Locate every Plasmodium vivax-infected red blood cell.
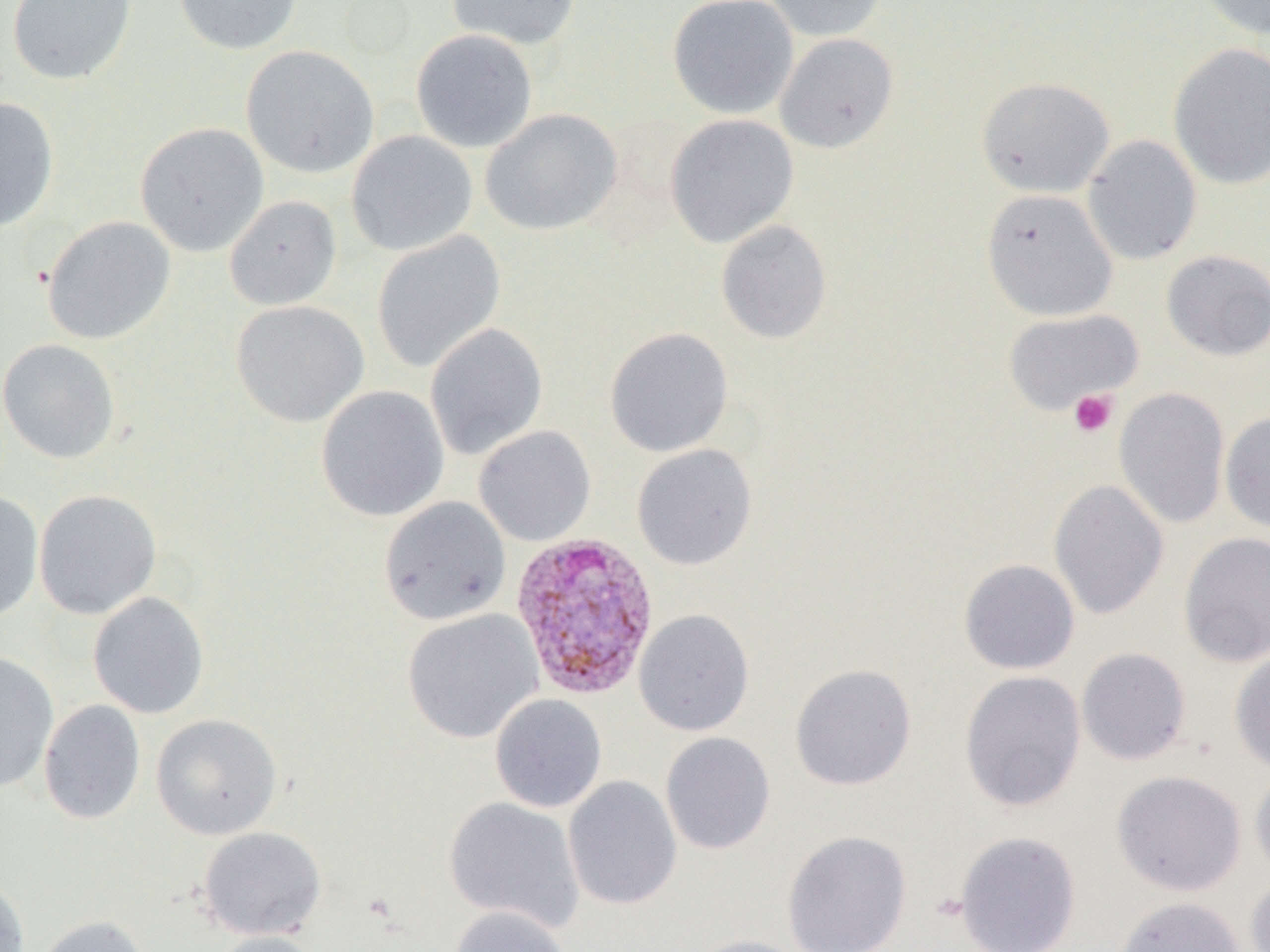

Approximate bounding boxes as (x1,y1)-(x2,y2) corner pairs in pixels.
Plasmodium vivax-infected red blood cells: (509,530)-(661,700).

slide_level_diagnosis: Plasmodium vivax
platelet_locations: 'approximate bounding boxes as (x1,y1)-(x2,y2) corner pairs in pixels: (1069,389)-(1118,438)'
image_size: 1270×952 pixels
preparation: thin blood film
magnification: 1000x
modality: light microscopy
field_of_view: single
uninfected_red_blood_cell_locations: 'approximate bounding boxes as (x1,y1)-(x2,y2) corner pairs in pixels: (7,0)-(137,86), (173,0)-(303,55), (446,0)-(581,51), (667,0)-(799,119), (763,0)-(889,42), (1194,0)-(1270,40), (410,29)-(538,153), (774,33)-(899,153), (1168,42)-(1270,190), (240,45)-(379,179), (975,76)-(1115,198), (0,96)-(59,232), (480,108)-(622,236), (665,114)-(799,248), (135,122)-(269,257), (346,130)-(478,256), (1082,134)-(1202,266), (981,189)-(1118,321), (224,195)-(342,310), (41,216)-(176,345), (715,219)-(832,344), (372,230)-(505,373), (1161,249)-(1270,361), (230,299)-(369,427), (1003,308)-(1143,414), (425,323)-(548,460), (604,327)-(734,458), (0,338)-(120,464), (316,385)-(449,522), (1114,386)-(1230,529), (1220,411)-(1270,534), (473,426)-(596,546), (631,443)-(758,570), (1048,479)-(1169,620), (33,489)-(162,619), (0,491)-(44,623), (379,496)-(511,626), (1178,531)-(1270,667), (959,558)-(1080,674), (88,591)-(209,719), (402,609)-(543,743), (633,609)-(754,736), (1076,647)-(1192,766), (1229,647)-(1270,774), (0,650)-(59,793), (790,663)-(917,791), (959,670)-(1086,812), (490,693)-(607,813), (39,699)-(145,824), (151,713)-(283,840), (660,732)-(776,855), (1249,766)-(1270,882), (1111,770)-(1247,896), (563,775)-(682,910), (443,796)-(585,932), (197,826)-(327,940), (781,830)-(913,952), (954,830)-(1081,952), (1244,874)-(1270,952), (0,875)-(31,952), (1111,895)-(1248,952), (451,906)-(571,952), (35,914)-(153,952), (207,931)-(326,952), (683,935)-(815,952)'